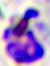
modality: micrograph
identification: white blood cell
magnification: 400x